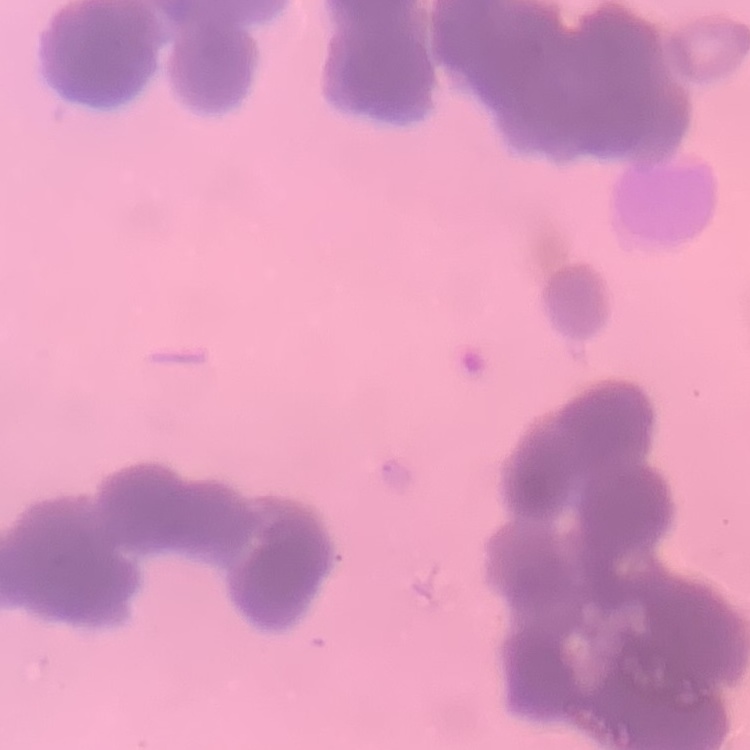
{
  "red_blood_cell_morphology": "rouleaux formation",
  "stain": "Field's or Giemsa",
  "preparation": "thin blood smear",
  "image_type": "square crop of a larger photomicrograph"
}